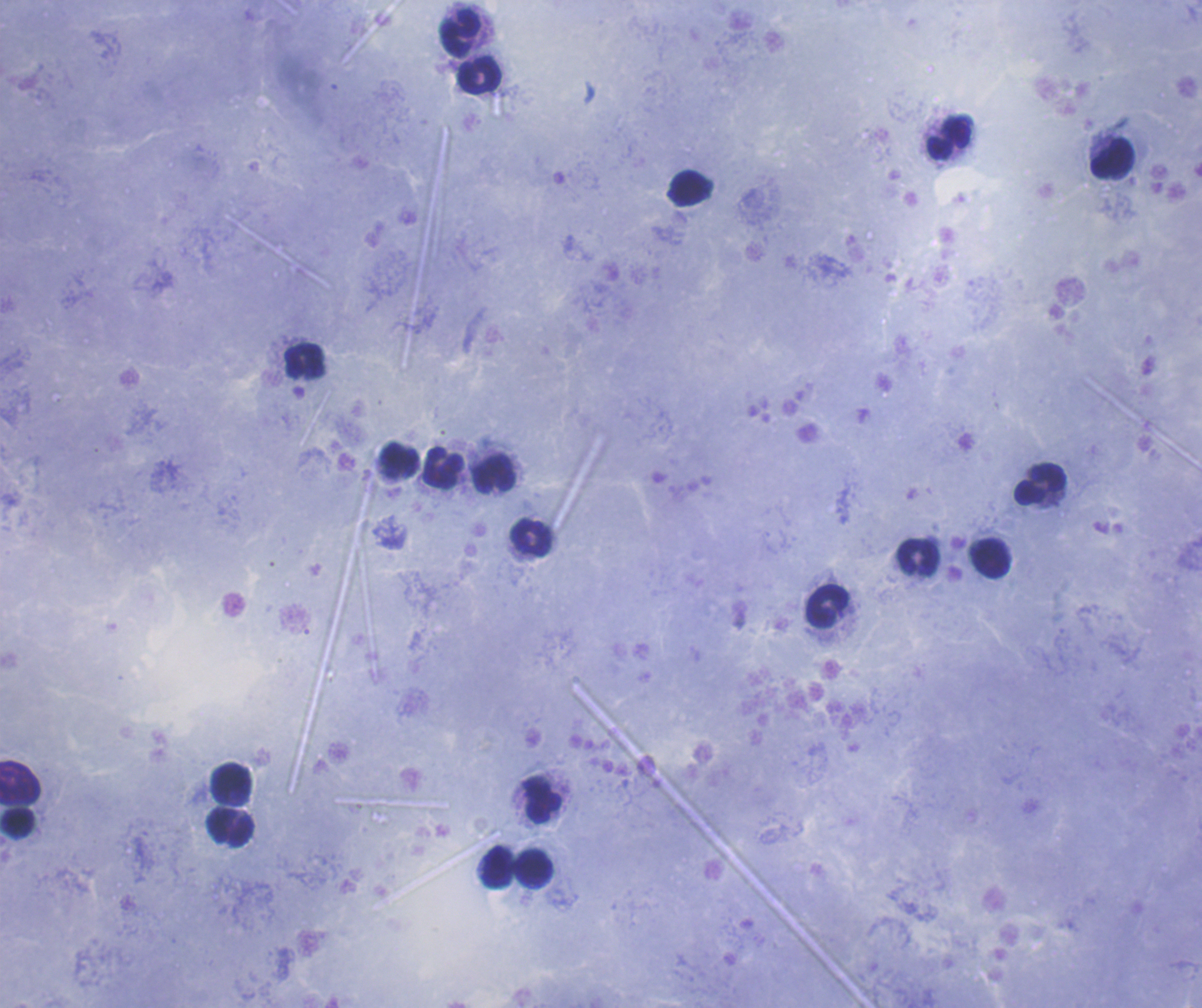
coordinate format = approximate centers as (x, y) in pixels
leukocyte locations = (461, 33), (479, 75), (949, 137), (1112, 158), (690, 187), (303, 361), (399, 460), (442, 468), (494, 473), (1040, 484), (531, 537), (919, 556), (991, 558), (827, 605), (231, 781), (19, 783), (543, 801), (18, 822), (231, 828), (497, 867), (534, 869)
context = previously used in an actual diagnosis
magnification = 100x
preparation = thick blood film
field of view = single
stain = Romanowsky
image size = 1202×1008 pixels
background quality = good
result = no Plasmodium parasites detected
coloration quality = good